State which parasite is depicted.
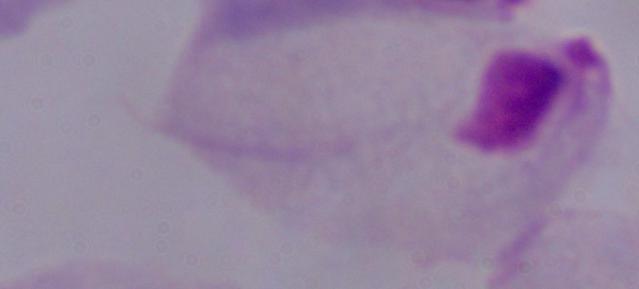

A trichomonad.

modality: photomicrograph
magnification: 1000x